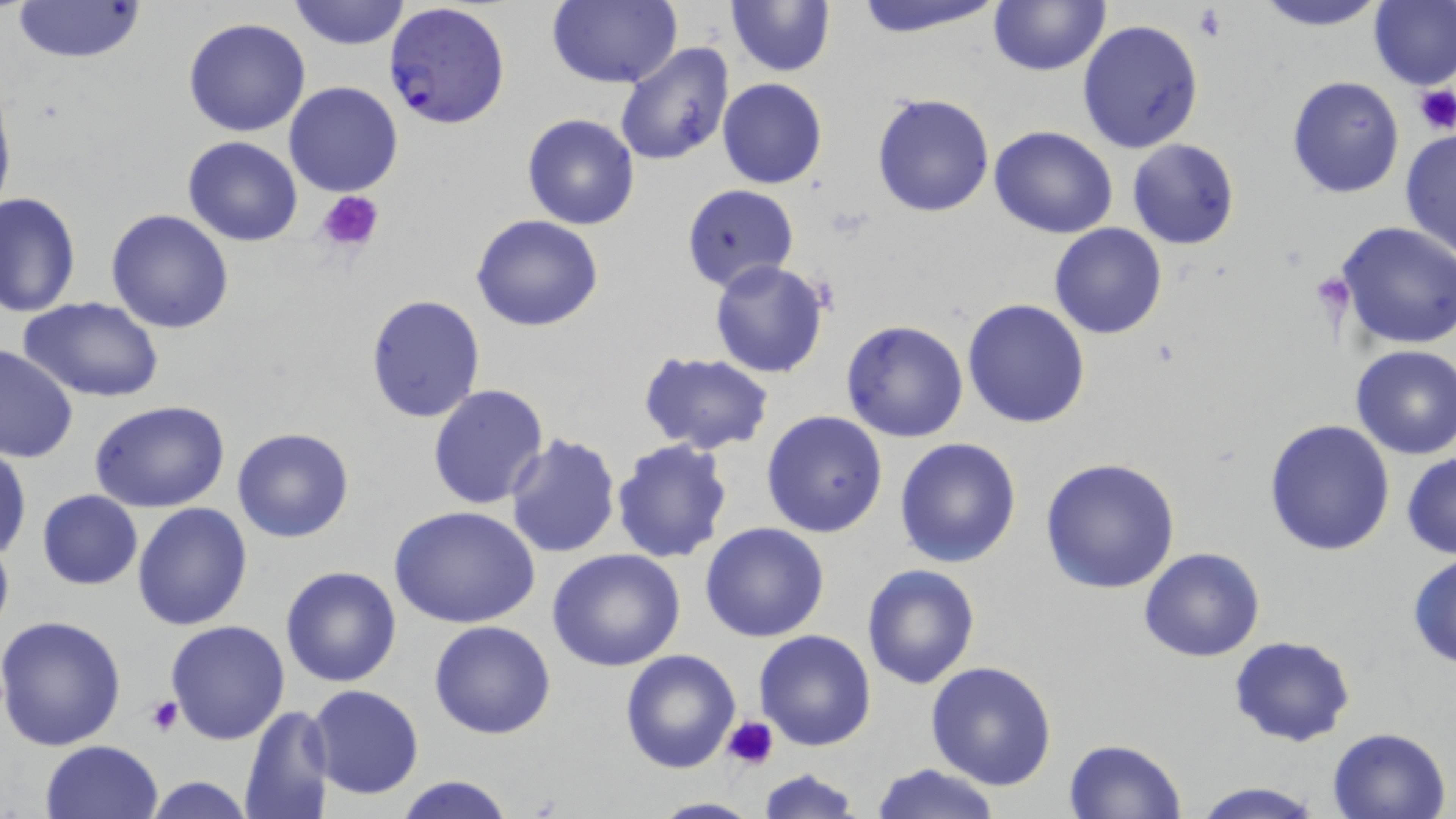

slide-level diagnosis = Plasmodium falciparum
modality = optical microscopy
image size = 1456×819 pixels
platelet locations = approximate bounding boxes as named x1/y1/x2/y2 corners in pixels: (x1=1193, y1=6, x2=1225, y2=41), (x1=1413, y1=83, x2=1456, y2=134), (x1=315, y1=190, x2=385, y2=253), (x1=147, y1=696, x2=183, y2=737), (x1=725, y1=715, x2=779, y2=771)
Plasmodium falciparum-infected red blood cell locations = approximate bounding boxes as named x1/y1/x2/y2 corners in pixels: (x1=383, y1=1, x2=511, y2=130)
stain = May-Grünwald-Giemsa
uninfected red blood cell locations = approximate bounding boxes as named x1/y1/x2/y2 corners in pixels: (x1=286, y1=0, x2=410, y2=49), (x1=546, y1=0, x2=679, y2=88), (x1=848, y1=0, x2=1008, y2=39), (x1=987, y1=0, x2=1111, y2=76), (x1=1249, y1=0, x2=1390, y2=31), (x1=1370, y1=0, x2=1456, y2=90), (x1=10, y1=1, x2=148, y2=64), (x1=725, y1=1, x2=836, y2=76), (x1=184, y1=17, x2=310, y2=137), (x1=1077, y1=19, x2=1205, y2=155), (x1=613, y1=41, x2=736, y2=167), (x1=1286, y1=76, x2=1404, y2=199), (x1=717, y1=78, x2=827, y2=189), (x1=0, y1=81, x2=16, y2=224), (x1=284, y1=81, x2=403, y2=197), (x1=871, y1=92, x2=995, y2=217), (x1=521, y1=113, x2=639, y2=230), (x1=989, y1=126, x2=1119, y2=239), (x1=1399, y1=127, x2=1456, y2=263), (x1=182, y1=137, x2=302, y2=247), (x1=1127, y1=138, x2=1240, y2=250), (x1=680, y1=184, x2=799, y2=291), (x1=1, y1=191, x2=81, y2=318), (x1=106, y1=208, x2=234, y2=333), (x1=470, y1=214, x2=605, y2=331), (x1=1049, y1=222, x2=1168, y2=341), (x1=1334, y1=222, x2=1456, y2=352), (x1=709, y1=258, x2=830, y2=378), (x1=364, y1=295, x2=487, y2=423), (x1=19, y1=298, x2=163, y2=402), (x1=962, y1=298, x2=1091, y2=428), (x1=840, y1=320, x2=970, y2=443), (x1=0, y1=344, x2=77, y2=464), (x1=1349, y1=346, x2=1456, y2=460), (x1=639, y1=352, x2=773, y2=456), (x1=428, y1=383, x2=550, y2=509), (x1=91, y1=401, x2=229, y2=513), (x1=761, y1=409, x2=889, y2=538), (x1=1264, y1=418, x2=1396, y2=557), (x1=231, y1=426, x2=355, y2=543), (x1=503, y1=432, x2=623, y2=558), (x1=611, y1=437, x2=734, y2=564), (x1=895, y1=438, x2=1022, y2=570), (x1=0, y1=447, x2=30, y2=561), (x1=1401, y1=451, x2=1456, y2=559), (x1=1039, y1=456, x2=1181, y2=594), (x1=37, y1=489, x2=143, y2=589), (x1=132, y1=502, x2=253, y2=631), (x1=391, y1=507, x2=539, y2=629), (x1=700, y1=523, x2=830, y2=643), (x1=546, y1=548, x2=685, y2=672), (x1=1138, y1=548, x2=1266, y2=662), (x1=1406, y1=553, x2=1456, y2=670), (x1=861, y1=563, x2=981, y2=689), (x1=279, y1=565, x2=403, y2=687), (x1=0, y1=616, x2=128, y2=753), (x1=166, y1=620, x2=290, y2=743), (x1=429, y1=620, x2=556, y2=739), (x1=755, y1=630, x2=875, y2=751), (x1=1230, y1=636, x2=1357, y2=748), (x1=620, y1=649, x2=741, y2=772), (x1=926, y1=661, x2=1057, y2=790), (x1=309, y1=684, x2=424, y2=800), (x1=239, y1=703, x2=334, y2=819), (x1=1328, y1=726, x2=1452, y2=819), (x1=1062, y1=739, x2=1187, y2=819), (x1=39, y1=740, x2=165, y2=819), (x1=869, y1=762, x2=1002, y2=819), (x1=756, y1=768, x2=862, y2=819), (x1=392, y1=775, x2=516, y2=819), (x1=139, y1=776, x2=257, y2=818), (x1=1186, y1=780, x2=1328, y2=819), (x1=644, y1=796, x2=766, y2=818)
magnification = 1000x
field of view = single
preparation = thin blood smear